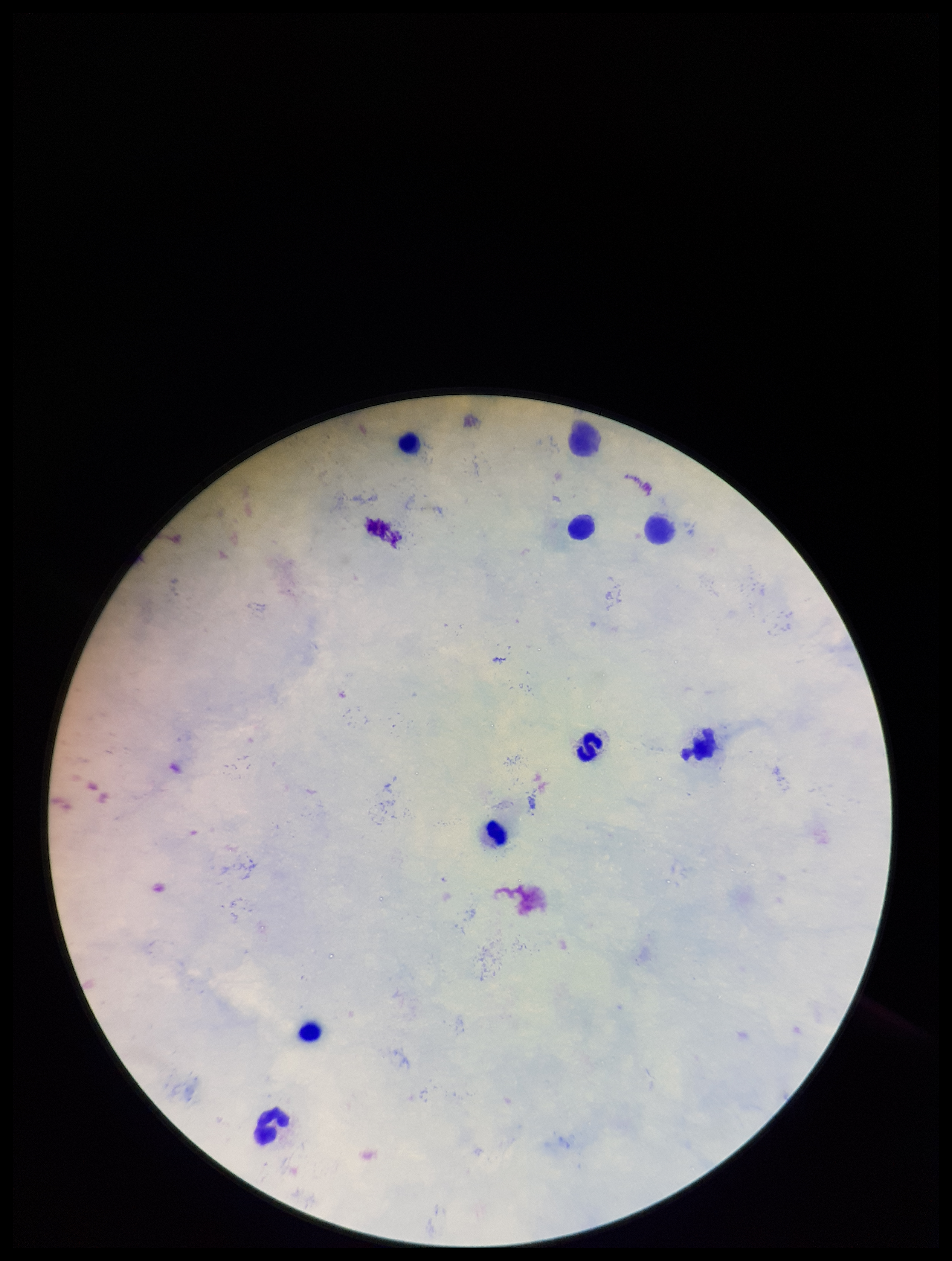 Giemsa stain. Parasite count: 0. Plasmodium parasites: none identified. Image is 952×1261 pixels. Leukocyte count: 9. Patient malaria status: negative. Preparation: thick smear. Photographed through the microscope eyepiece with a smartphone camera. One field from this slide.